Name the parasite shown.
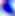
This is Toxoplasma gondii.

Micrograph. Captured at 400x magnification.